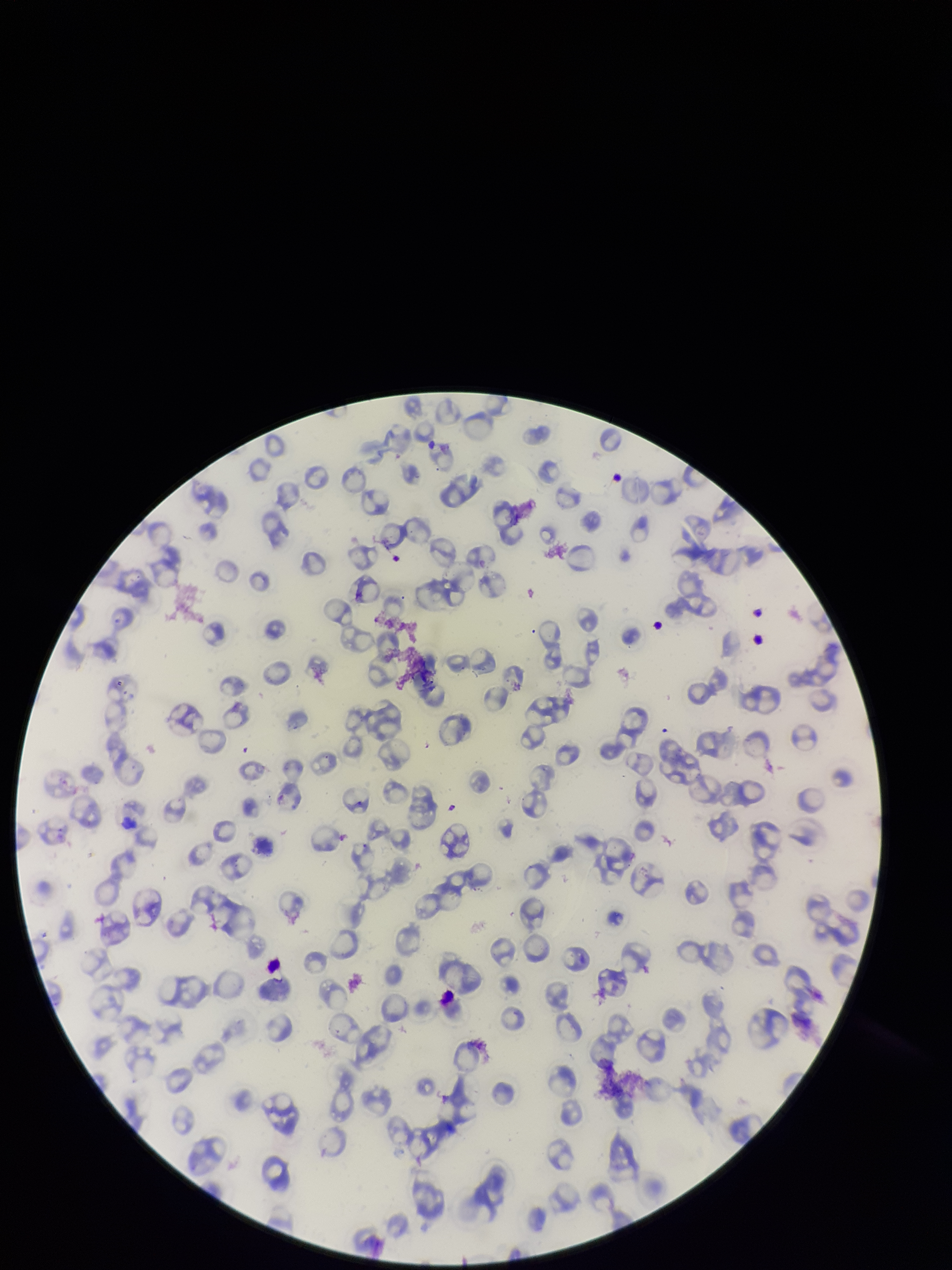
Summary:
  - Field of view: single
  - Patient malaria status: infected
  - Species reported for this patient: Plasmodium falciparum
  - Parasitized red blood cells: none identified
  - Stain: Giemsa
  - Parasitized red blood cell count: 0
  - Red blood cell count: 96
  - Image size: 952×1270 pixels
  - Capture: smartphone photograph through the microscope eyepiece
  - Preparation: thin blood smear